Locate every leukocyte (white blood cell).
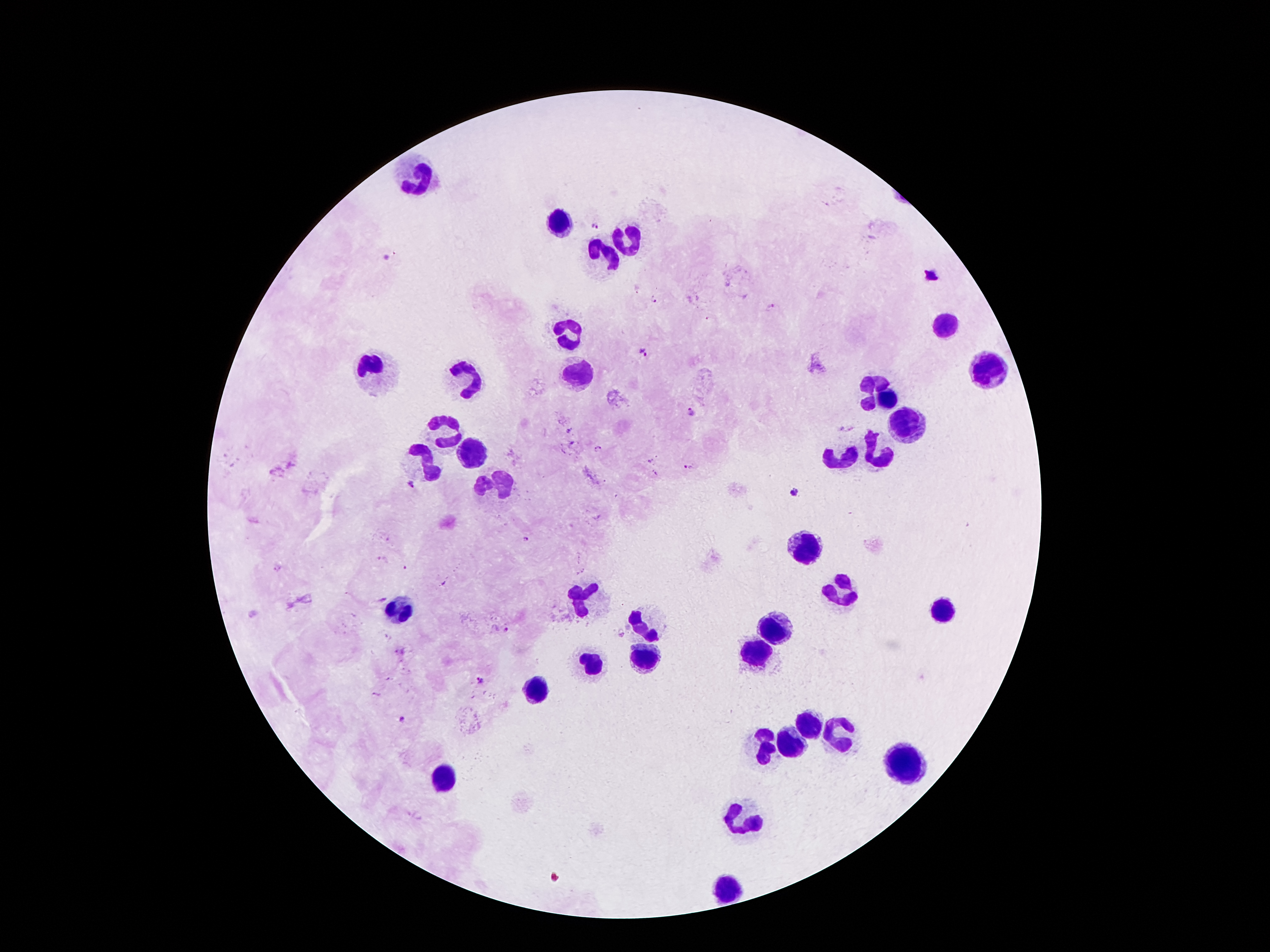

Approximate centers as [x, y] in pixels.
Leukocytes: [416, 178], [560, 225], [625, 243], [601, 257], [946, 327], [570, 334], [368, 367], [990, 372], [573, 374], [467, 381], [865, 383], [884, 400], [908, 421], [445, 432], [467, 453], [875, 453], [419, 461], [845, 461], [494, 483], [806, 550], [843, 593], [580, 597], [405, 608], [946, 608], [638, 623], [778, 628], [754, 651], [646, 655], [589, 658], [535, 692], [808, 725], [834, 731], [791, 746], [761, 748], [899, 761], [444, 780], [746, 819], [731, 886].

Summary:
  - Malaria parasite locations: [594, 226], [654, 300], [772, 304], [646, 352], [690, 410], [598, 449], [687, 464], [411, 484], [793, 493], [523, 538], [383, 599], [504, 630], [480, 678], [379, 692], [400, 718]
  - Field of view: one from this slide
  - Preparation: thick blood film
  - Capture: smartphone camera through the microscope eyepiece
  - Patient malaria status: infected with Plasmodium falciparum
  - Image size: 1270×952 pixels
  - Magnification: 100x
  - Stain: Giemsa